Classify this cell by malaria status.
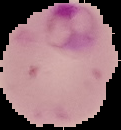

It is parasitized.

Summary:
  - Image size: 121×130 pixels
  - Preparation: thin blood smear
  - Image type: segmented cell region on a black background